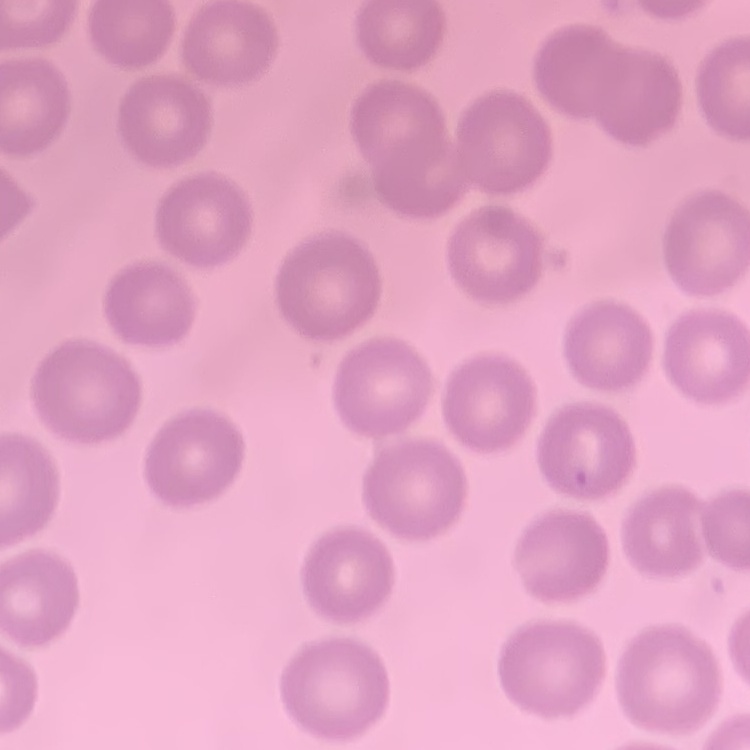 The erythrocytes exhibit no rouleaux formation. Stained with either Field's or Giemsa. One tile cut from a larger photomicrograph. Thin peripheral smear.